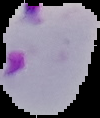

From a thin blood film. Image is 100×118 pixels. Result: malaria parasites identified. Cell region segmented out of the field of view; the surrounding area is masked to black.